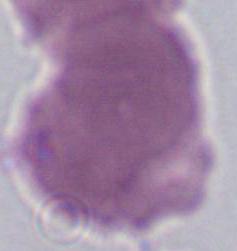

{
  "identification": "erythrocyte",
  "magnification": "1000x",
  "modality": "micrograph"
}